Report the malaria status of this cell.
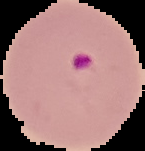

Parasitized.

Summary:
  - Preparation: thin blood film
  - Image type: segmented cell region on a black background
  - Image size: 145×151 pixels